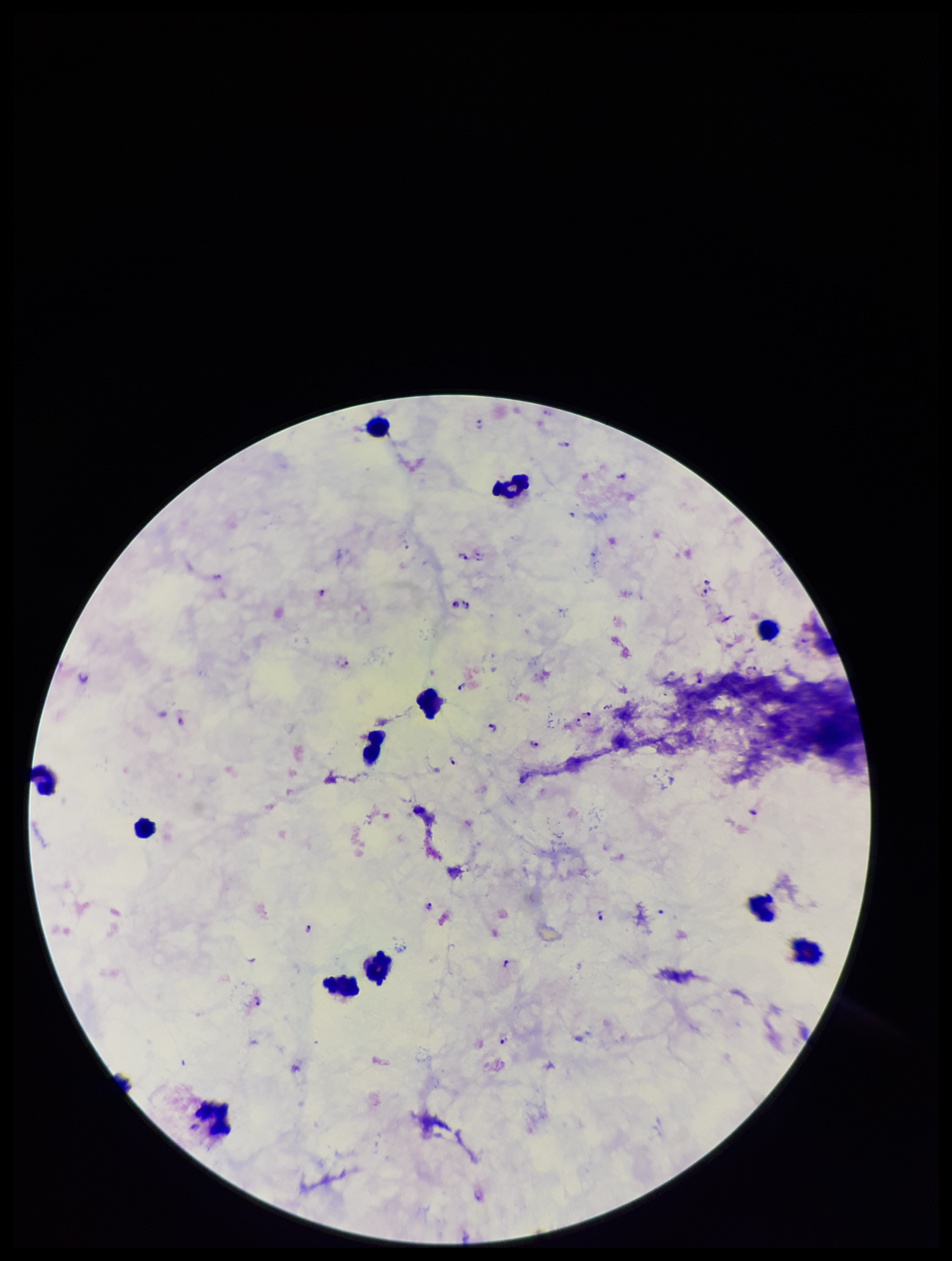

Summary:
  - Plasmodium parasites: detected
  - Species reported for this patient: Plasmodium falciparum
  - Capture: smartphone photograph through the microscope eyepiece
  - Stain: Giemsa
  - Preparation: thick
  - Patient malaria status: positive
  - Field of view: single
  - Parasite count: 20
  - Leukocyte count: 12
  - Image size: 952×1261 pixels